Report the malaria status of this cell.
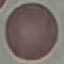

Uninfected.

Thin blood film. Giemsa-stained preparation. Photographed with a smartphone camera at the microscope eyepiece. Cell patch, automatically extracted from a larger field of view and resized to 64 × 64 pixels.